Classify this cell by malaria status.
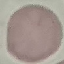
Uninfected.

preparation: thin smear
stain: Giemsa
capture: smartphone through the microscope eyepiece
image_type: cell patch, automatically extracted from a larger field of view and resized to 64 × 64 pixels